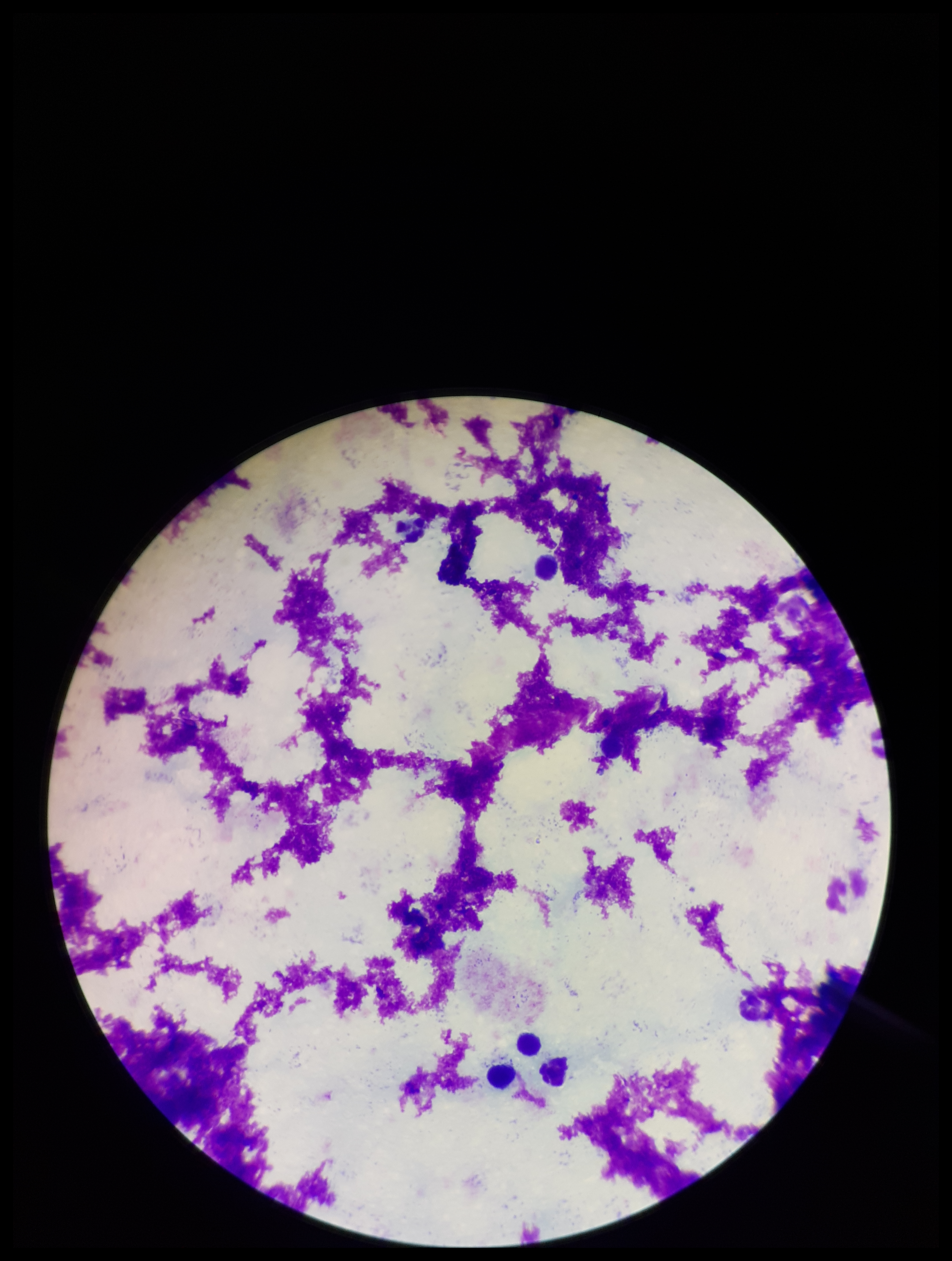 Leukocyte count: 4. Stained with Giemsa. Preparation: thick smear. Image is 952×1261 pixels. One field from this slide. Plasmodium parasites: none seen. Patient malaria status: negative. Smartphone photograph taken through the eyepiece of a microscope. Parasite count: 0.